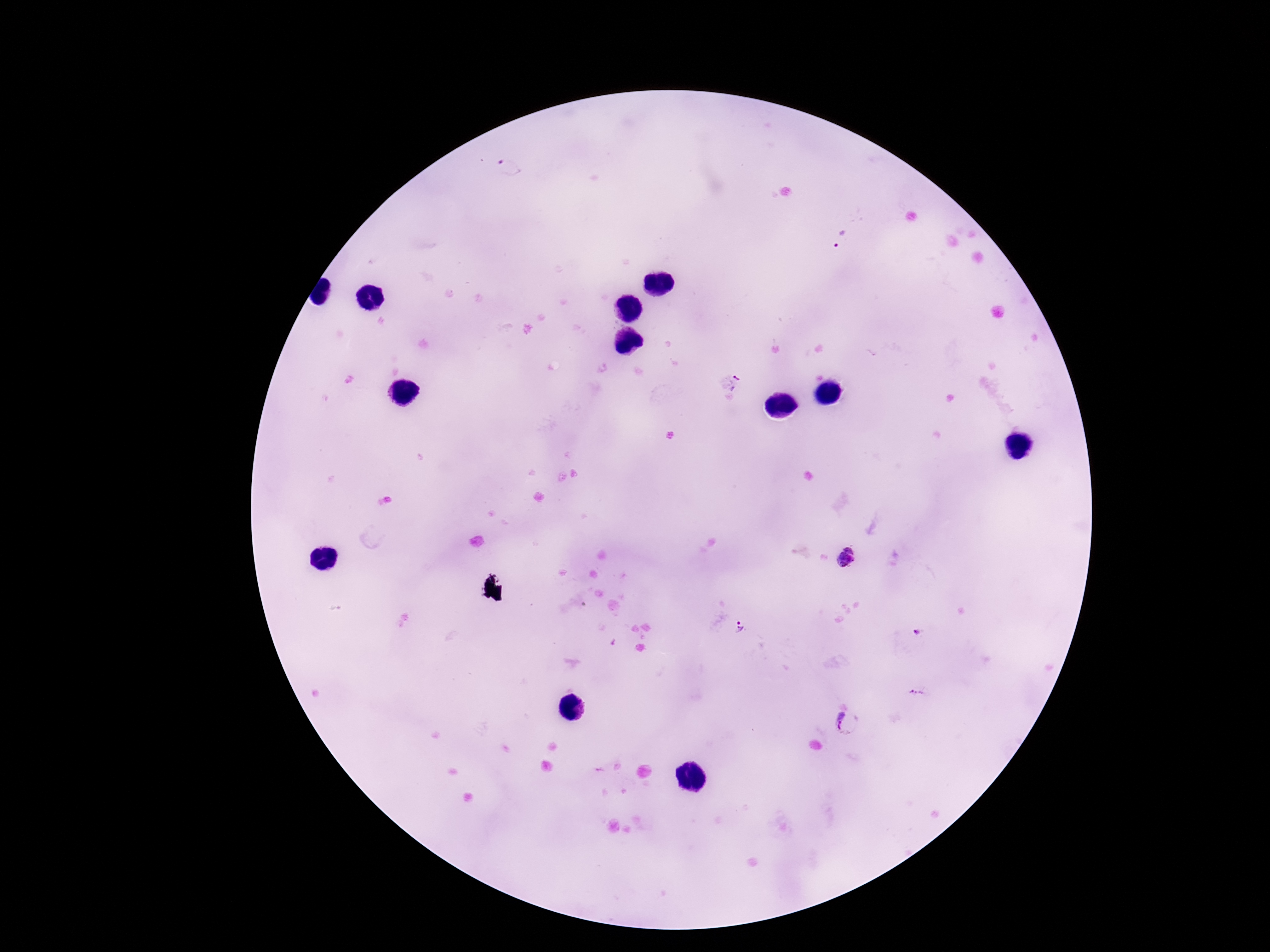

Approximate centers as (x, y) in pixels.
Summary:
  - Plasmodium parasite locations: (507, 166), (844, 240), (727, 382), (848, 558), (738, 629), (918, 633), (918, 694), (848, 723)
  - Preparation: thick blood film
  - Patient malaria status: positive
  - Stain: Giemsa
  - Capture: smartphone camera through the microscope eyepiece
  - Field of view: one from this slide
  - Magnification: 100x
  - Image size: 1270×952 pixels